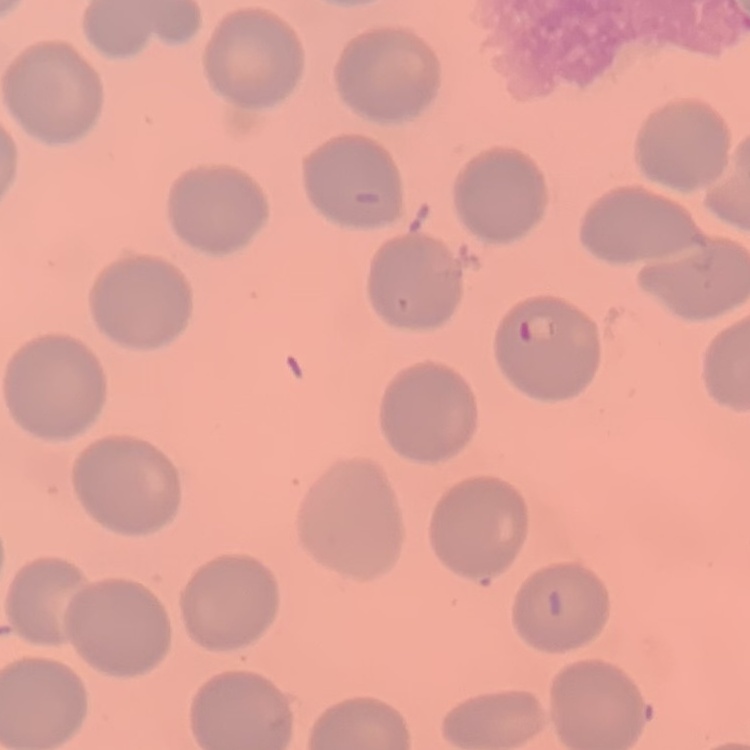

Summary:
  - Red blood cell morphology: no rouleaux formation
  - Stain: Field's or Giemsa
  - Image type: one tile cut from a larger photomicrograph
  - Preparation: thin peripheral smear